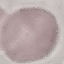

malaria status = uninfected
image type = automatically extracted cell patch, resized to 64 × 64 pixels
stain = Giemsa
preparation = thin blood smear
capture = smartphone through the microscope eyepiece